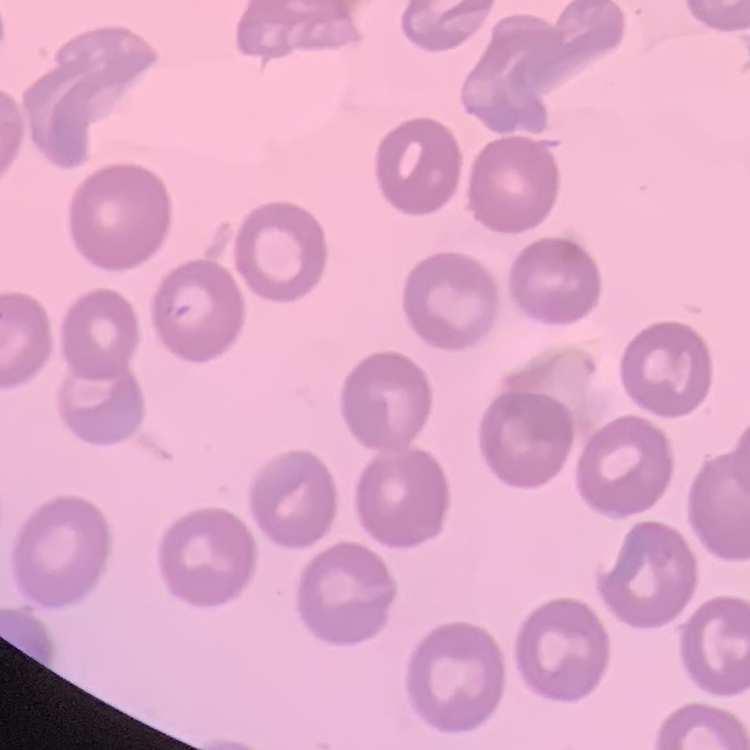

Summary:
  - Red blood cell morphology: no rouleaux formation
  - Stain: Field's or Giemsa
  - Image type: one tile cut from a larger photomicrograph
  - Preparation: thin blood smear